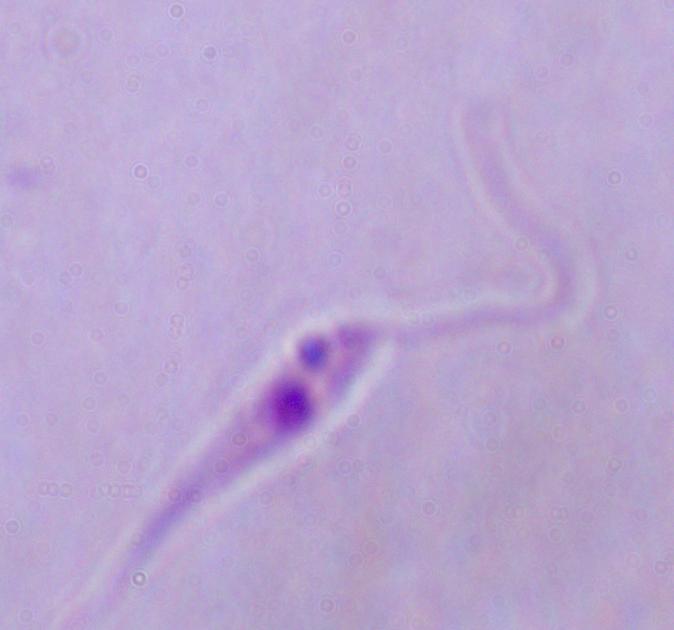

Captured at 1000x magnification. Micrograph. A Leishmania parasite is shown.